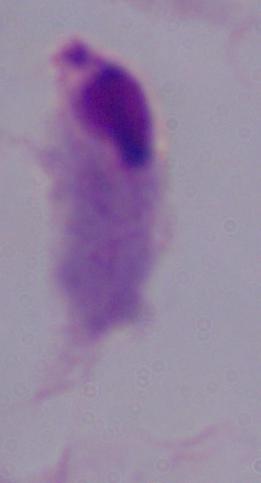

A trichomonad is seen. Captured at 1000x magnification. Photomicrograph.